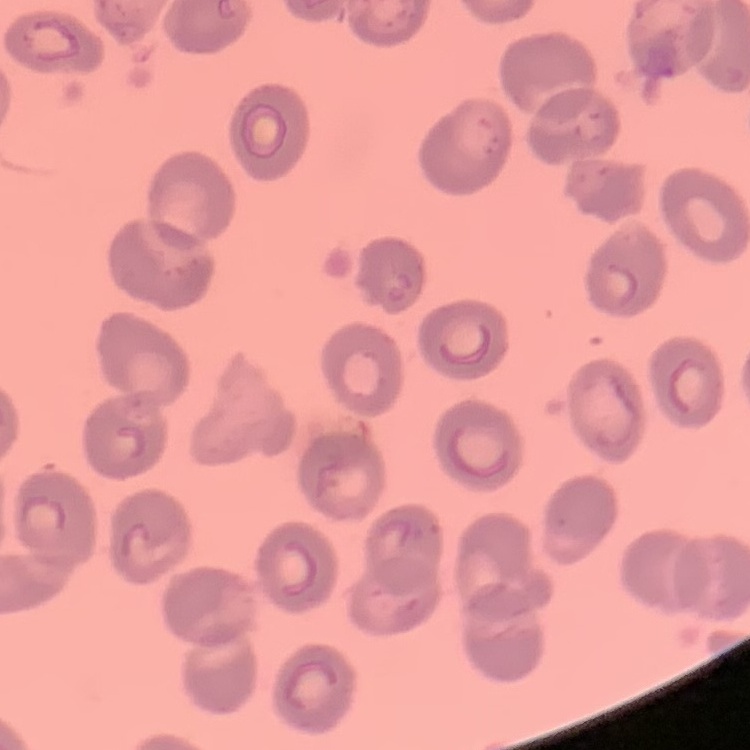
Summary:
  - Erythrocyte morphology: no rouleaux formation
  - Preparation: thin blood film
  - Stain: Field's or Giemsa
  - Image type: one tile cut from a larger photomicrograph